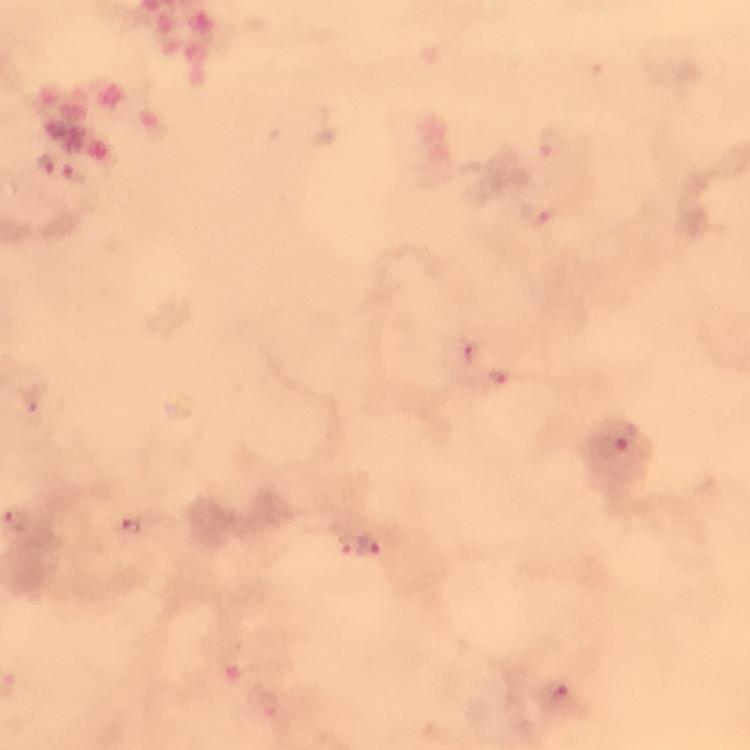

Approximate centers as {x, y} in pixels. Plasmodium parasite locations: {548, 143}, {534, 215}, {463, 349}, {501, 377}, {613, 446}, {19, 522}, {132, 530}, {349, 544}, {371, 545}, {553, 690}, {268, 706}. Smartphone photograph taken through a microscope. Image is 750×750 pixels. 100x magnification. Giemsa-stained preparation. Thick blood smear. A crop from one field of view. From a malaria diagnostic workup. Immersion oil was used.